Assess this cell for malaria.
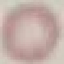

Uninfected.

Giemsa stain. Thin blood film. Acquired by smartphone through the microscope eyepiece. Cell patch, automatically extracted from a larger field of view and resized to 64 × 64 pixels.